Outline platelets.
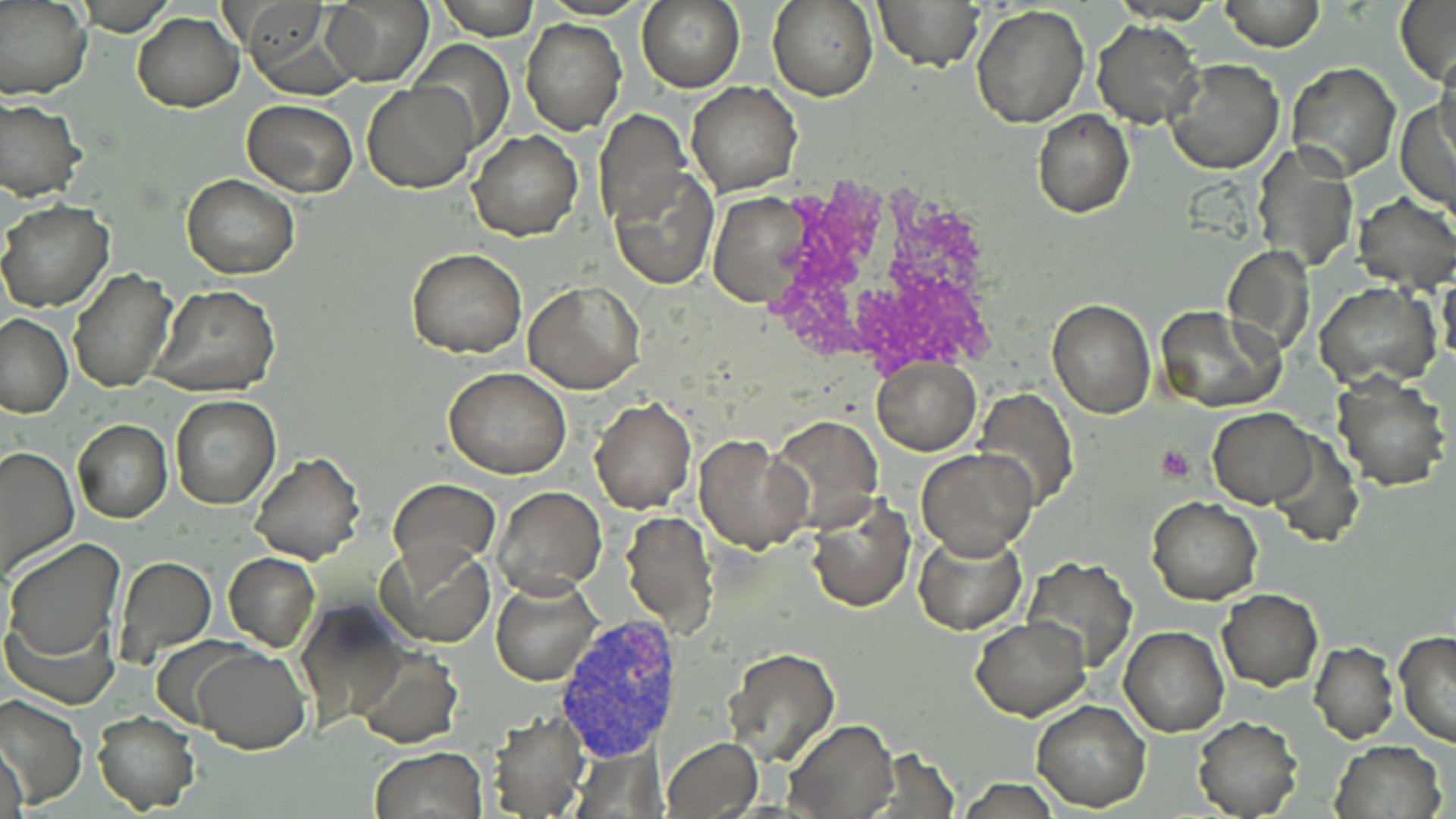
Approximate bounding boxes as (x1,y1)-(x2,y2) corner pairs in pixels.
Platelets: (1155,443)-(1196,485).

slide-level diagnosis = Plasmodium vivax
modality = light microscopy
magnification = 1000x
image size = 1456×819 pixels
white blood cell locations = approximate bounding boxes as (x1,y1)-(x2,y2) corner pairs in pixels: (758,176)-(999,375)
field of view = one of a larger specimen
preparation = thin blood film
stain = May-Grünwald-Giemsa
uninfected red blood cell locations = approximate bounding boxes as (x1,y1)-(x2,y2) corner pairs in pixels: (0,0)-(93,101), (436,0)-(538,40), (637,0)-(744,92), (768,0)-(878,101), (874,0)-(983,71), (1223,0)-(1322,51), (1394,0)-(1456,88), (321,1)-(432,85), (971,6)-(1090,127), (131,12)-(242,110), (245,12)-(358,99), (520,18)-(625,135), (1093,20)-(1205,129), (408,38)-(515,157), (1432,51)-(1456,152), (1165,58)-(1284,176), (1285,63)-(1400,180), (686,81)-(803,197), (363,83)-(476,193), (1396,95)-(1455,214), (0,99)-(86,201), (242,100)-(357,195), (593,110)-(690,232), (1031,110)-(1134,218), (468,130)-(583,240), (1250,143)-(1359,273), (608,164)-(717,290), (181,175)-(300,279), (708,193)-(812,307), (1355,194)-(1456,292), (0,201)-(116,312), (1223,246)-(1316,357), (408,249)-(526,358), (69,269)-(174,393), (1440,270)-(1456,371), (524,280)-(645,393), (1315,283)-(1440,388), (151,285)-(279,396), (1046,300)-(1155,418), (1155,304)-(1284,414), (0,314)-(75,418), (871,359)-(981,454), (443,368)-(571,479), (1331,372)-(1451,491), (973,389)-(1079,513), (169,394)-(280,509), (589,396)-(697,514), (1208,408)-(1316,508), (769,416)-(884,534), (74,420)-(171,522), (1269,431)-(1365,548), (694,435)-(811,554), (0,444)-(78,577), (915,448)-(1038,560), (251,453)-(364,565), (389,478)-(500,575), (494,486)-(605,596), (808,497)-(915,614), (1148,497)-(1262,604), (620,512)-(718,635), (913,529)-(1027,636), (3,536)-(125,676), (378,543)-(493,645), (224,553)-(320,651), (1024,556)-(1137,672), (116,557)-(216,658), (491,575)-(602,687), (1217,589)-(1322,690), (295,600)-(407,732), (972,617)-(1090,720), (1119,625)-(1228,736), (1395,632)-(1456,748), (1310,642)-(1398,744), (189,645)-(310,752), (722,647)-(841,767), (354,648)-(463,748), (1,694)-(87,809), (1032,701)-(1151,812), (90,711)-(200,813), (485,712)-(590,819), (1193,715)-(1303,819), (783,719)-(898,819), (661,737)-(762,817), (1329,740)-(1447,819), (1,741)-(30,819), (369,746)-(487,819), (956,778)-(1065,817)
Plasmodium vivax-infected red blood cell locations = approximate bounding boxes as (x1,y1)-(x2,y2) corner pairs in pixels: (553,618)-(685,764)